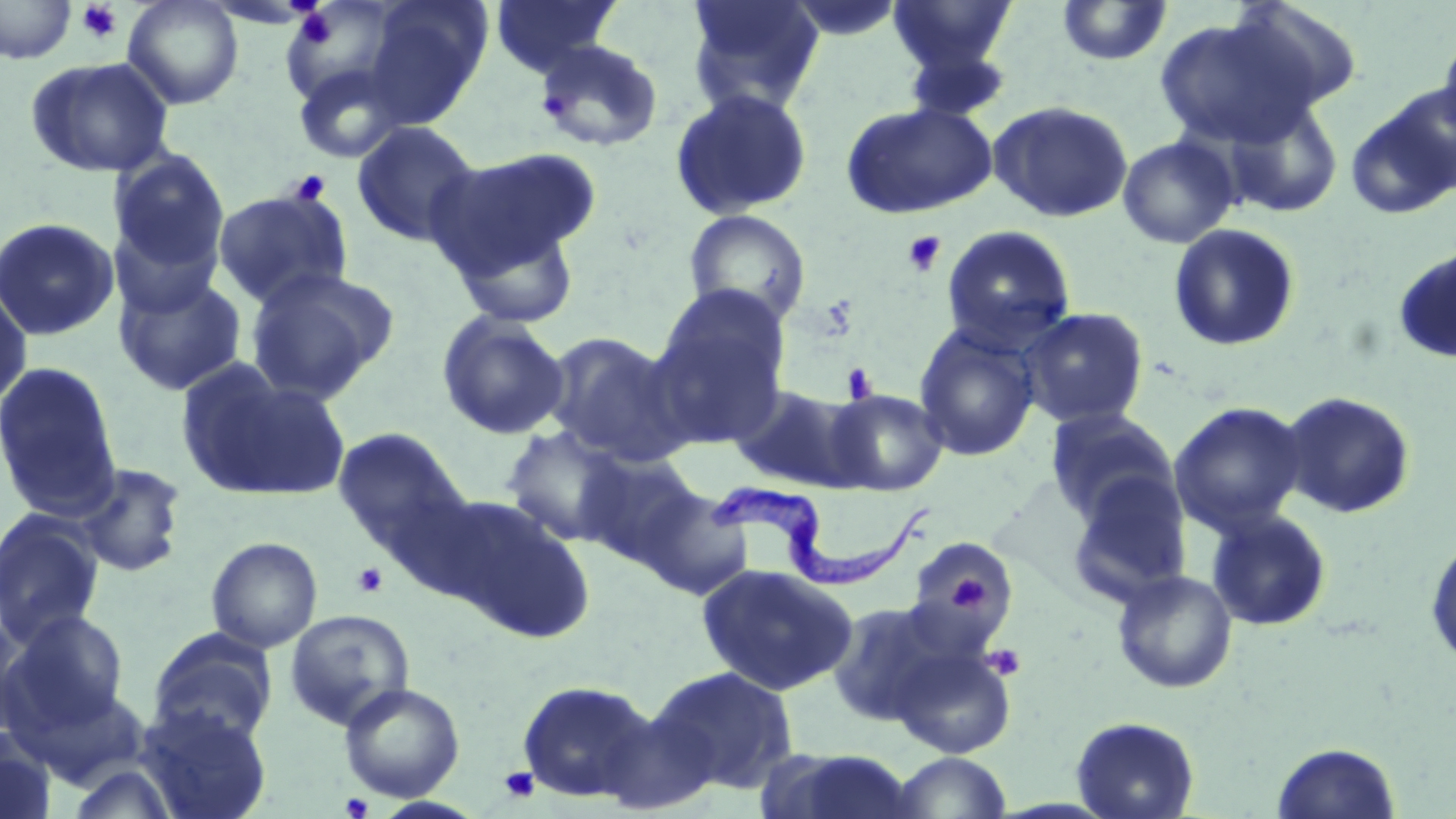
Approximate bounding boxes as (x1,y1)-(x2,y2) corner pairs in pixels. Platelet locations: (75,1)-(124,43), (294,8)-(337,48), (288,170)-(331,205), (902,231)-(946,277), (841,363)-(879,404), (352,562)-(388,598), (945,570)-(994,615), (983,644)-(1025,681), (499,767)-(540,803), (341,792)-(373,818). Trypanosoma brucei locations: (711,479)-(938,587). Uninfected red blood cell locations: (122,0)-(244,110), (490,0)-(621,78), (684,0)-(826,116), (888,0)-(1017,75), (0,1)-(78,65), (361,1)-(491,129), (782,1)-(906,43), (1056,1)-(1173,66), (1225,1)-(1366,114), (1154,17)-(1314,148), (1438,31)-(1456,150), (534,38)-(664,152), (900,45)-(1013,123), (25,56)-(176,178), (292,61)-(409,164), (669,88)-(813,221), (1345,90)-(1456,220), (1220,96)-(1344,218), (989,100)-(1134,223), (841,101)-(997,219), (351,120)-(482,247), (1117,135)-(1240,249), (109,147)-(230,280), (428,147)-(597,279), (212,187)-(354,309), (682,209)-(812,329), (0,218)-(120,341), (108,219)-(224,319), (452,221)-(582,330), (1168,223)-(1300,352), (940,224)-(1077,352), (1392,246)-(1456,364), (244,266)-(399,403), (113,270)-(248,397), (0,283)-(33,412), (648,287)-(791,448), (1019,307)-(1149,429), (436,311)-(570,441), (913,323)-(1041,461), (542,331)-(691,466), (0,361)-(123,520), (178,363)-(350,503), (728,384)-(868,493), (826,388)-(948,496), (1278,390)-(1417,519), (1169,402)-(1307,536), (1044,407)-(1180,525), (500,426)-(632,546), (331,427)-(471,560), (577,450)-(705,566), (73,462)-(188,578), (1065,473)-(1194,606), (634,485)-(755,600), (437,497)-(596,644), (1206,509)-(1333,632), (1,510)-(106,648), (1424,532)-(1456,673), (206,536)-(323,653), (904,539)-(1017,643), (696,563)-(857,696), (1111,569)-(1239,693), (826,600)-(956,727), (3,609)-(130,734), (284,609)-(415,731), (0,614)-(36,741), (147,628)-(277,746), (890,642)-(1016,758), (646,665)-(800,796), (516,679)-(658,803), (339,682)-(465,802), (136,704)-(272,819), (597,704)-(721,814), (1071,715)-(1199,819), (0,729)-(58,819), (1271,741)-(1402,818), (767,748)-(920,819), (890,752)-(1012,818), (65,762)-(182,819). Slide-level diagnosis: Trypanosoma brucei. Captured at 1000x magnification. Thin blood film. May-Grünwald-Giemsa stain. Optical microscopy. Single field of view. Image is 1456×819 pixels.